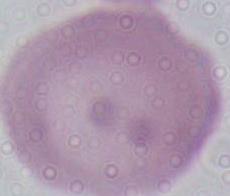

Captured at 1000x magnification. A red blood cell is seen. Micrograph.